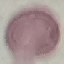
Malaria status: uninfected. Photographed with a smartphone camera at the microscope eyepiece. Thin blood film. Giemsa stain. Cell patch, automatically extracted from a larger field of view and resized to 64 × 64 pixels.